Give the preparation type.
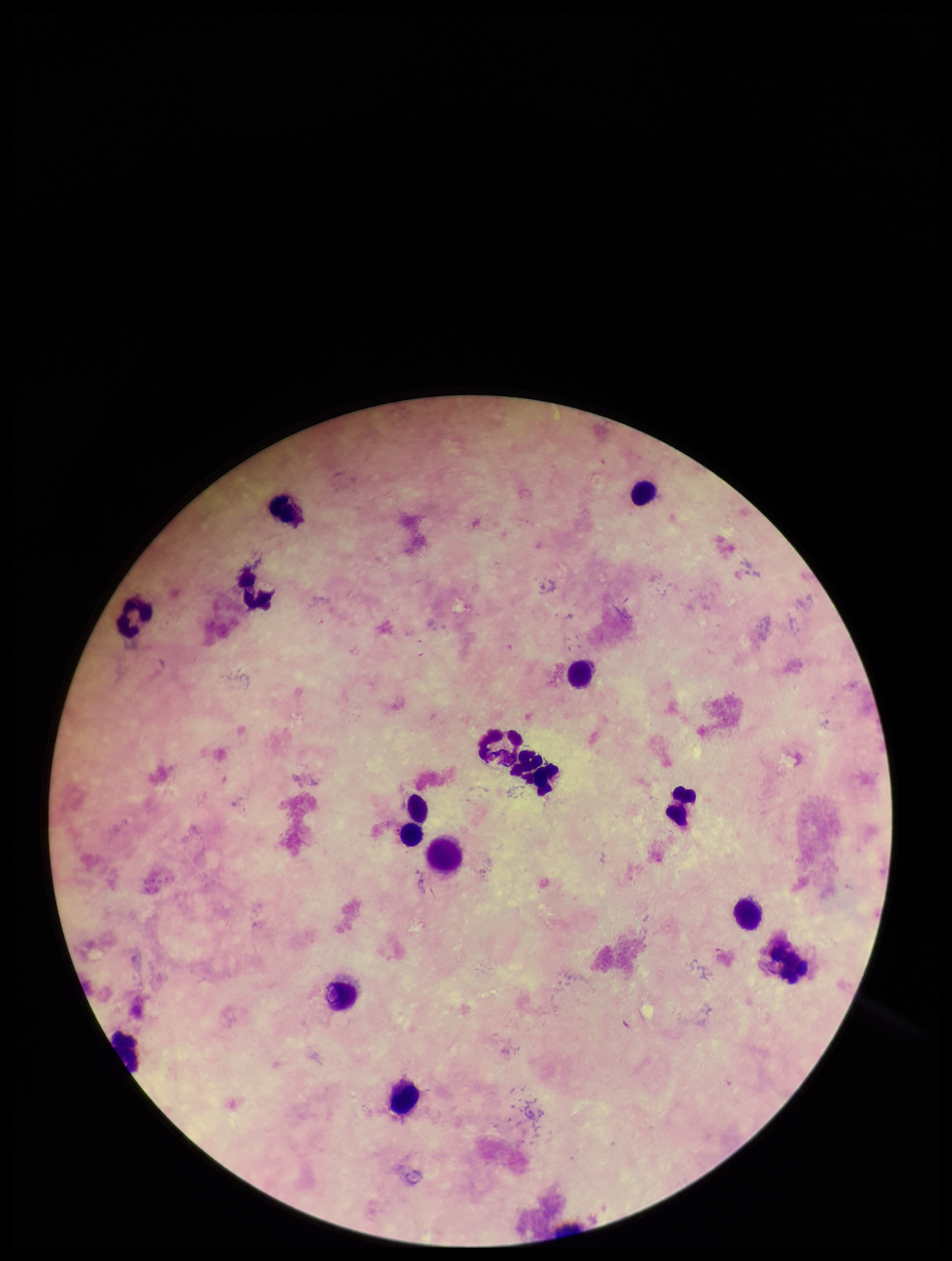

Thick.

Plasmodium parasites: none seen. Leukocyte count: 15. Image is 952×1261 pixels. Parasite count: 0. Photographed through the microscope eyepiece with a smartphone camera. Single field of view. Patient malaria status: negative. Stained with Giemsa.